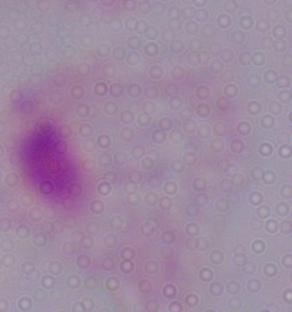
magnification = 1000x
identification = trichomonad
modality = micrograph